Mark where platelets are.
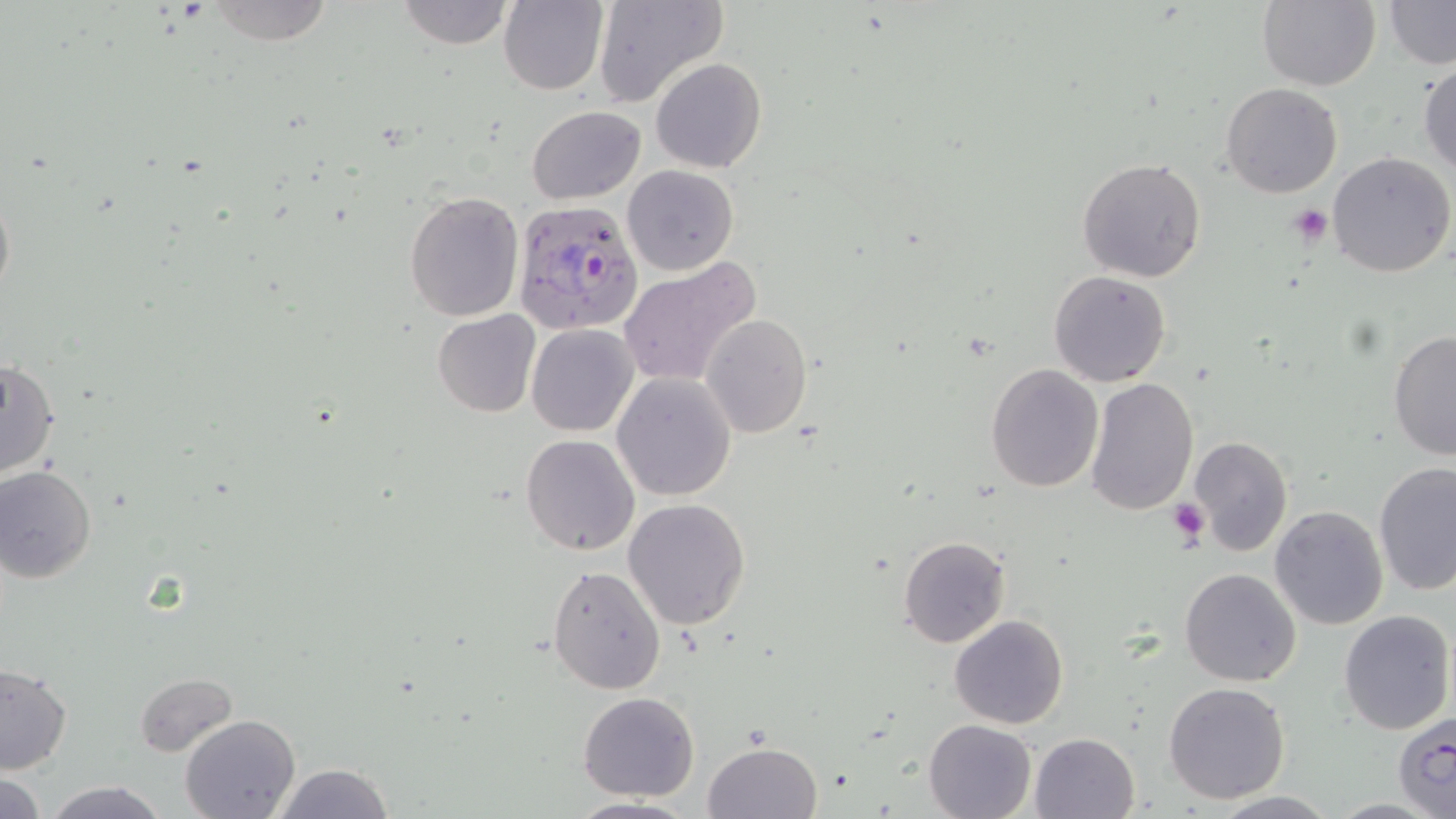
Approximate bounding boxes as [x1, y1, x2, y2] in pixels.
Platelets: [1288, 205, 1334, 247], [1169, 499, 1208, 546].

Plasmodium falciparum-infected red blood cell locations: [510, 199, 646, 339], [1391, 711, 1456, 819]. Uninfected red blood cell locations: [394, 0, 514, 48], [499, 0, 609, 95], [591, 0, 726, 109], [1258, 0, 1381, 91], [1381, 0, 1455, 69], [201, 2, 338, 43], [650, 58, 767, 173], [1418, 62, 1456, 177], [1221, 83, 1344, 198], [526, 105, 646, 203], [1326, 152, 1455, 278], [1076, 157, 1206, 283], [623, 165, 738, 275], [404, 190, 525, 322], [617, 260, 760, 388], [1048, 269, 1172, 388], [432, 310, 540, 417], [700, 315, 813, 440], [526, 323, 639, 436], [1388, 328, 1456, 461], [0, 357, 61, 479], [986, 364, 1104, 493], [611, 372, 736, 500], [1084, 378, 1197, 516], [1189, 434, 1293, 558], [520, 435, 640, 555], [1373, 461, 1456, 597], [0, 465, 97, 584], [623, 498, 750, 630], [1269, 505, 1390, 630], [897, 536, 1011, 648], [547, 564, 667, 694], [1178, 567, 1302, 686], [1338, 608, 1454, 734], [950, 613, 1069, 729], [0, 664, 72, 775], [134, 672, 239, 757], [1163, 681, 1290, 804], [578, 692, 701, 802], [179, 714, 302, 819], [923, 718, 1037, 819], [1030, 732, 1141, 819], [702, 741, 823, 819], [268, 761, 398, 818], [0, 772, 46, 818], [44, 780, 169, 819], [1206, 792, 1341, 819], [566, 795, 700, 818]. Slide-level diagnosis: Plasmodium falciparum. May-Grünwald-Giemsa stain. Image is 1456×819 pixels. Thin blood film. Single field of view. Captured at 1000x magnification. Optical microscopy.